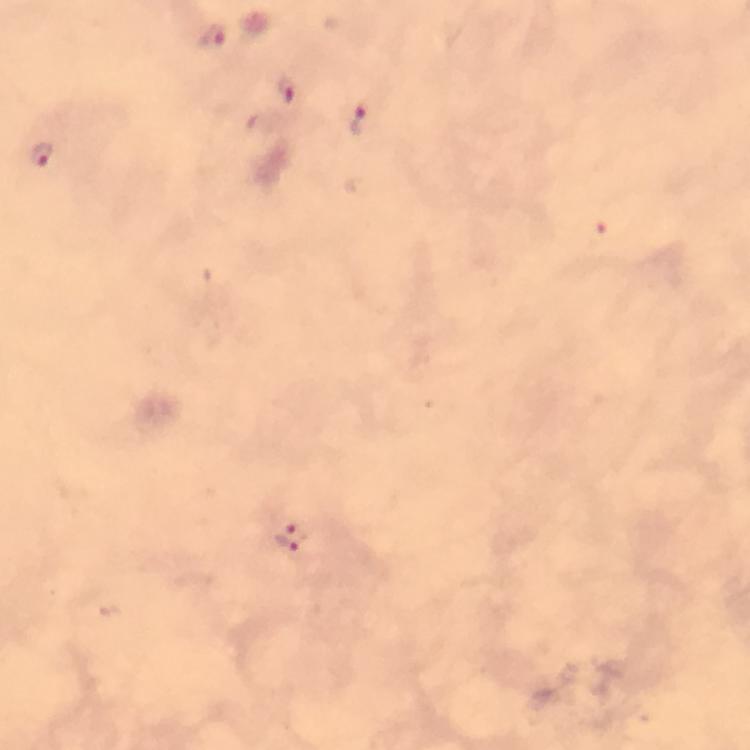
{
  "image_size": "750×750 pixels",
  "stain": "Giemsa",
  "preparation": "thick blood film",
  "magnification": "100x",
  "context": "from a malaria diagnostic workup",
  "capture": "smartphone camera through the microscope",
  "immersion_oil": "used",
  "malaria_parasite_locations": "approximate centers as (x, y) in pixels: (213, 36), (285, 89), (360, 120), (41, 154), (289, 535)",
  "cropped_from": "one field of view"
}